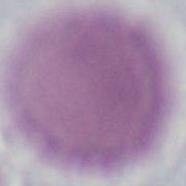

{
  "modality": "photomicrograph",
  "magnification": "1000x",
  "identification": "erythrocyte"
}